Identify the blood parasite species.
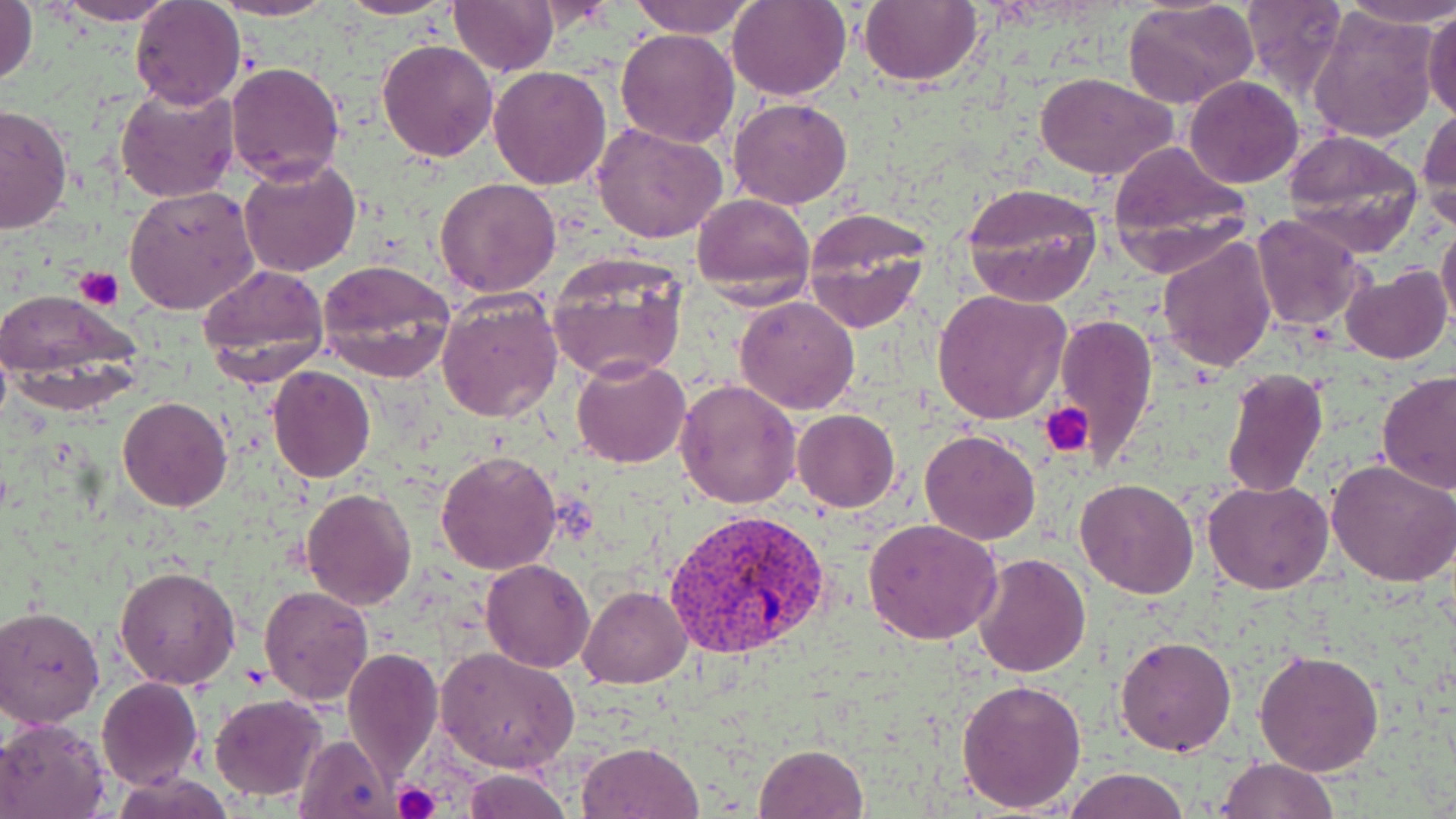

Plasmodium vivax.

Approximate bounding boxes as (x1, y1, x2, y2) in pixels. Plasmodium vivax-infected red blood cell locations: (666, 507, 833, 659). Uninfected red blood cell locations: (50, 0, 181, 24), (339, 0, 455, 20), (448, 0, 559, 76), (628, 0, 758, 40), (727, 0, 851, 100), (859, 0, 983, 88), (1237, 0, 1348, 100), (1339, 0, 1456, 29), (130, 1, 246, 111), (213, 1, 340, 21), (1123, 2, 1261, 111), (1, 3, 38, 90), (1424, 6, 1456, 122), (1306, 7, 1440, 145), (615, 27, 742, 147), (378, 40, 498, 162), (226, 62, 344, 184), (488, 64, 613, 189), (1036, 72, 1177, 180), (1184, 76, 1304, 188), (115, 84, 238, 204), (729, 97, 852, 209), (0, 104, 73, 234), (1418, 107, 1456, 228), (593, 122, 730, 245), (1282, 130, 1425, 254), (1105, 140, 1247, 249), (238, 159, 361, 277), (434, 177, 563, 297), (962, 181, 1104, 306), (124, 186, 260, 316), (692, 194, 815, 305), (802, 210, 932, 332), (1250, 214, 1369, 333), (1437, 221, 1456, 335), (1157, 236, 1277, 373), (547, 255, 690, 383), (317, 261, 455, 381), (197, 264, 331, 385), (1341, 266, 1452, 365), (0, 289, 137, 388), (931, 289, 1072, 423), (436, 291, 563, 425), (734, 296, 860, 415), (1053, 312, 1158, 468), (571, 358, 691, 470), (269, 365, 375, 483), (1220, 367, 1328, 500), (1374, 371, 1456, 495), (674, 378, 802, 508), (118, 396, 233, 512), (791, 409, 900, 512), (919, 428, 1042, 545), (435, 450, 562, 576), (1327, 459, 1456, 589), (1075, 478, 1199, 599), (1203, 480, 1334, 594), (299, 486, 417, 611), (862, 519, 1005, 645), (971, 553, 1092, 678), (481, 559, 596, 672), (113, 566, 241, 690), (259, 585, 373, 705), (577, 585, 691, 689), (0, 606, 104, 727), (1114, 634, 1237, 755), (436, 646, 580, 774), (340, 647, 444, 782), (1254, 649, 1385, 776), (97, 677, 203, 790), (957, 677, 1088, 813), (208, 693, 327, 802), (0, 716, 110, 818), (294, 732, 397, 818), (578, 741, 704, 819), (753, 744, 869, 818), (1215, 756, 1339, 818), (1063, 768, 1191, 819), (463, 769, 572, 819), (117, 775, 230, 819). Platelet locations: (74, 267, 124, 310), (1041, 404, 1093, 456), (391, 781, 441, 819). May-Grünwald-Giemsa-stained preparation. Light microscopy. Thin blood film. One field of a larger specimen. Image is 1456×819 pixels. Captured at 1000x magnification.